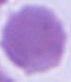

magnification = 1000x
identification = red blood cell
modality = photomicrograph